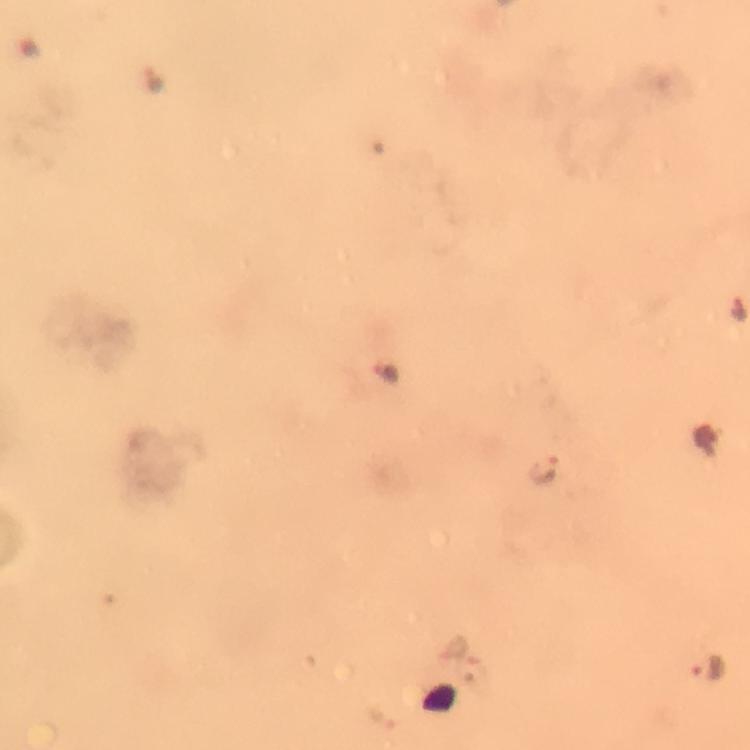
Approximate centers as [x, y] in pixels.
Summary:
  - Malaria parasite locations: [544, 467], [709, 665]
  - Stain: Giemsa
  - Cropped from: a single field of view
  - Image size: 750×750 pixels
  - Immersion oil: applied
  - Context: from a diagnostic examination for malaria
  - Capture: smartphone mounted on the microscope
  - Preparation: thick blood smear
  - Magnification: 100x